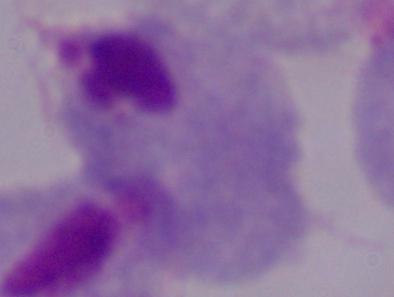
A trichomonad is shown. Micrograph. Captured at 1000x magnification.